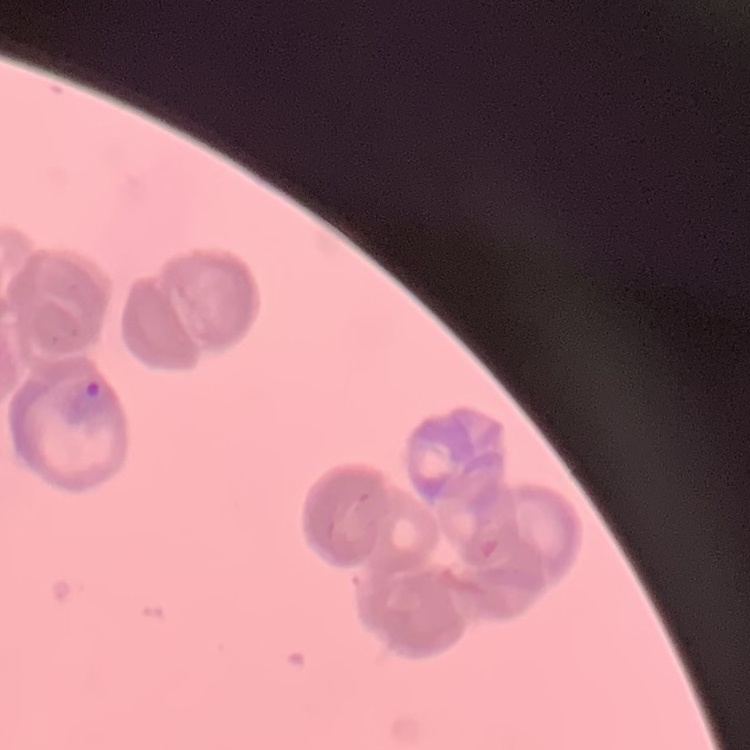 The erythrocytes exhibit rouleaux formation. Stained with either Field's or Giemsa. One tile cut from a larger photomicrograph. Thin blood smear.